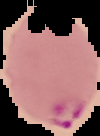

Summary:
  - Malaria status: parasitized
  - Image type: segmented cell region on a black background
  - Image size: 100×136 pixels
  - Preparation: thin blood smear